Locate every blood parasite and identify its species.
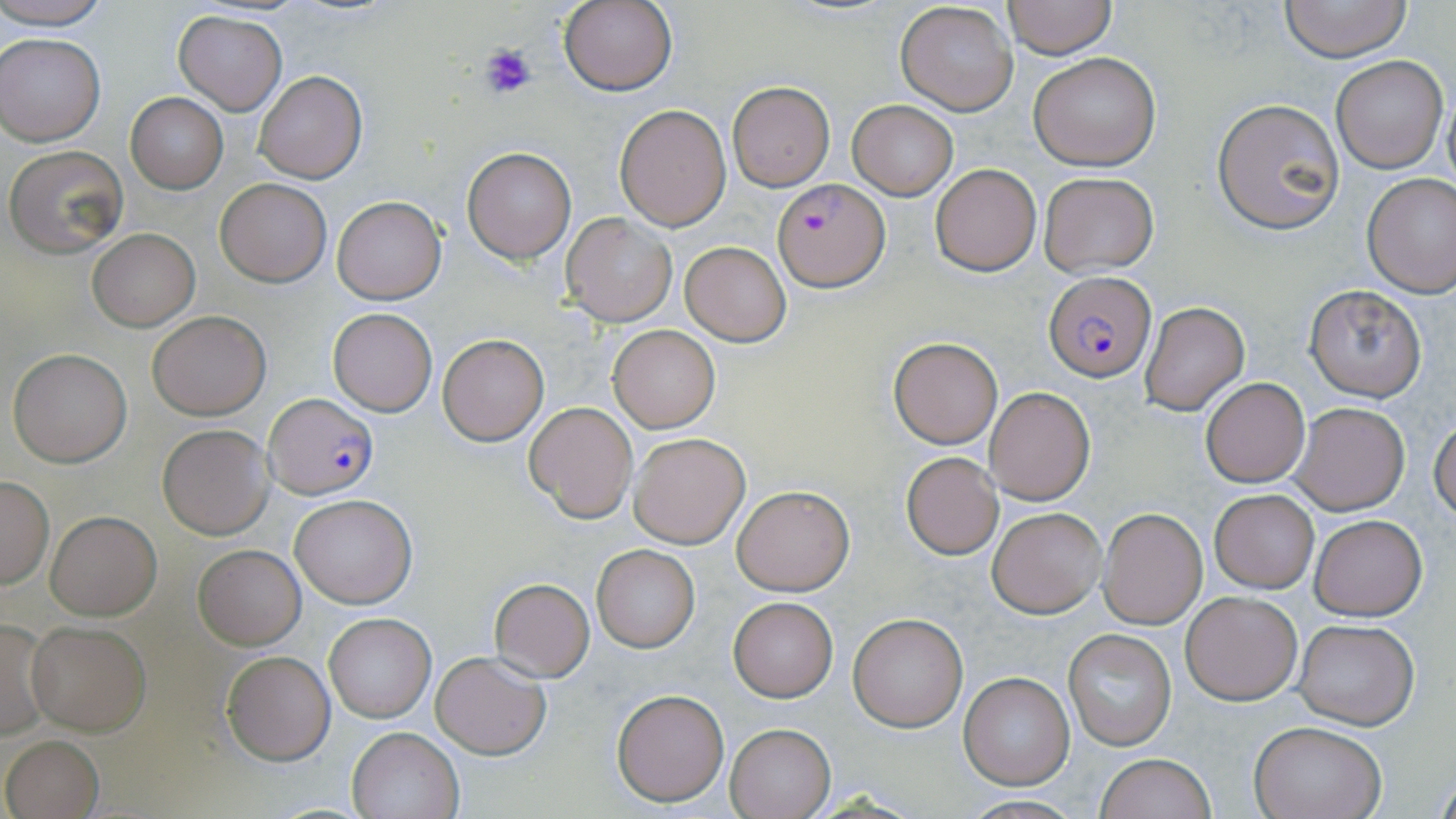
Approximate bounding boxes as named x1/y1/x2/y2 corners in pixels.
Plasmodium falciparum-infected red blood cells: (x1=772, y1=180, x2=888, y2=290), (x1=1044, y1=273, x2=1154, y2=382), (x1=265, y1=393, x2=379, y2=499).
No Plasmodium ovale, Plasmodium malariae, Plasmodium vivax, Babesia divergens, or Trypanosoma brucei observed.

{
  "slide_level_diagnosis": "Plasmodium falciparum",
  "stain": "May-Grünwald-Giemsa",
  "uninfected_red_blood_cell_locations": "approximate bounding boxes as named x1/y1/x2/y2 corners in pixels: (x1=0, y1=0, x2=113, y2=29), (x1=558, y1=0, x2=677, y2=95), (x1=1004, y1=0, x2=1115, y2=58), (x1=1278, y1=0, x2=1413, y2=62), (x1=895, y1=2, x2=1018, y2=116), (x1=172, y1=9, x2=287, y2=113), (x1=1, y1=33, x2=105, y2=146), (x1=1028, y1=53, x2=1161, y2=171), (x1=1331, y1=55, x2=1448, y2=174), (x1=254, y1=70, x2=368, y2=183), (x1=727, y1=82, x2=834, y2=190), (x1=1442, y1=84, x2=1456, y2=192), (x1=126, y1=94, x2=227, y2=194), (x1=1213, y1=97, x2=1345, y2=234), (x1=847, y1=100, x2=959, y2=199), (x1=613, y1=103, x2=731, y2=231), (x1=4, y1=145, x2=129, y2=256), (x1=461, y1=145, x2=576, y2=263), (x1=931, y1=164, x2=1041, y2=275), (x1=1039, y1=172, x2=1159, y2=274), (x1=1362, y1=174, x2=1456, y2=297), (x1=215, y1=178, x2=331, y2=286), (x1=332, y1=196, x2=446, y2=304), (x1=562, y1=213, x2=677, y2=326), (x1=87, y1=229, x2=199, y2=330), (x1=681, y1=242, x2=790, y2=346), (x1=1304, y1=284, x2=1428, y2=403), (x1=1141, y1=301, x2=1250, y2=415), (x1=328, y1=308, x2=438, y2=416), (x1=146, y1=311, x2=270, y2=420), (x1=607, y1=325, x2=720, y2=433), (x1=438, y1=334, x2=548, y2=445), (x1=889, y1=337, x2=1001, y2=448), (x1=7, y1=348, x2=131, y2=467), (x1=1201, y1=377, x2=1309, y2=486), (x1=984, y1=387, x2=1095, y2=504), (x1=1289, y1=401, x2=1411, y2=516), (x1=524, y1=402, x2=639, y2=523), (x1=1430, y1=416, x2=1456, y2=522), (x1=156, y1=423, x2=274, y2=539), (x1=628, y1=431, x2=750, y2=549), (x1=902, y1=453, x2=1002, y2=560), (x1=0, y1=477, x2=53, y2=586), (x1=733, y1=485, x2=854, y2=597), (x1=1210, y1=489, x2=1319, y2=594), (x1=290, y1=494, x2=418, y2=608), (x1=987, y1=506, x2=1106, y2=618), (x1=1098, y1=507, x2=1207, y2=629), (x1=45, y1=511, x2=162, y2=619), (x1=1309, y1=513, x2=1428, y2=620), (x1=194, y1=545, x2=306, y2=649), (x1=593, y1=546, x2=700, y2=652), (x1=488, y1=578, x2=595, y2=681), (x1=1182, y1=592, x2=1301, y2=705), (x1=729, y1=597, x2=837, y2=702), (x1=847, y1=611, x2=968, y2=732), (x1=324, y1=613, x2=435, y2=722), (x1=0, y1=618, x2=52, y2=739), (x1=1294, y1=618, x2=1418, y2=730), (x1=25, y1=619, x2=152, y2=734), (x1=1063, y1=629, x2=1178, y2=750), (x1=431, y1=650, x2=551, y2=759), (x1=222, y1=651, x2=335, y2=765), (x1=958, y1=673, x2=1074, y2=790), (x1=610, y1=688, x2=729, y2=806), (x1=1249, y1=721, x2=1386, y2=819), (x1=724, y1=723, x2=835, y2=818), (x1=347, y1=726, x2=464, y2=819), (x1=2, y1=734, x2=104, y2=818), (x1=1094, y1=753, x2=1217, y2=819)",
  "preparation": "thin blood film",
  "platelet_locations": "approximate bounding boxes as named x1/y1/x2/y2 corners in pixels: (x1=478, y1=43, x2=536, y2=102)",
  "modality": "light microscopy",
  "magnification": "1000x",
  "image_size": "1456×819 pixels",
  "field_of_view": "one of a larger specimen"
}